Identify the cell.
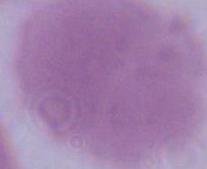
An erythrocyte.

Micrograph. Captured at 1000x magnification.